State which parasite is depicted.
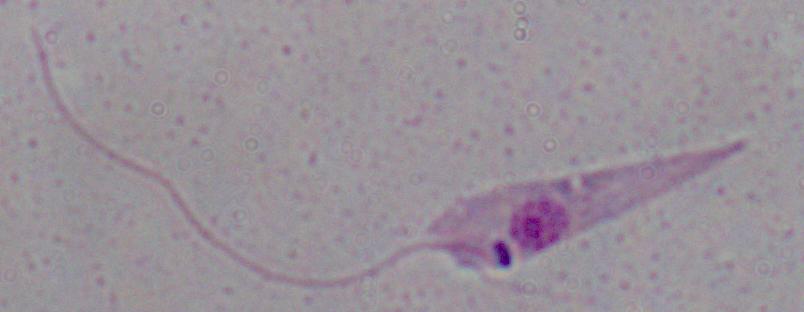
Leishmania.

magnification: 1000x
modality: photomicrograph